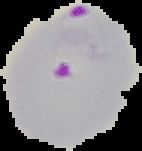 Cell region segmented out of the field of view; the surrounding area is masked to black. Image is 142×151 pixels. From a thin blood film. Malaria status: parasitized.